State which cell type is depicted.
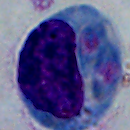
This is a leukocyte.

modality = micrograph
magnification = 1000x